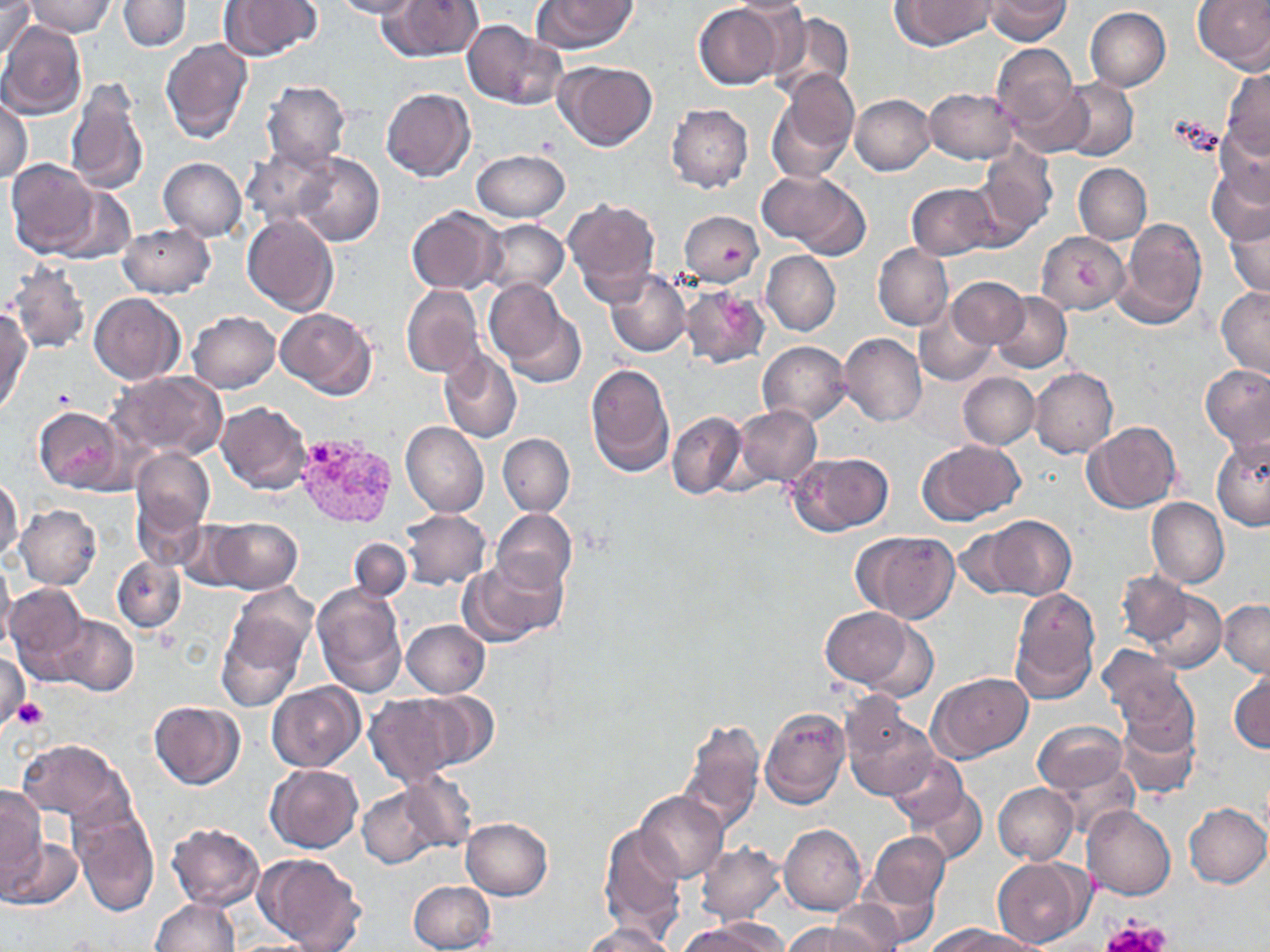 Approximate bounding boxes as [x1, y1, x2, y2] in pixels. Plasmodium vivax-infected red blood cell locations: [291, 432, 399, 531]. Platelet locations: [1173, 114, 1224, 156], [721, 242, 747, 271], [720, 299, 752, 331], [10, 697, 48, 728], [1103, 913, 1174, 952]. Uninfected red blood cell locations: [1, 0, 37, 64], [23, 0, 116, 37], [331, 0, 421, 19], [381, 0, 484, 62], [531, 0, 638, 54], [725, 0, 814, 18], [890, 0, 995, 50], [984, 0, 1070, 45], [1193, 0, 1270, 72], [118, 1, 190, 52], [219, 1, 321, 62], [694, 3, 785, 90], [1085, 6, 1171, 91], [767, 10, 855, 101], [0, 21, 87, 119], [461, 21, 565, 109], [160, 38, 252, 144], [992, 44, 1079, 136], [553, 61, 659, 152], [1221, 67, 1270, 157], [773, 69, 858, 173], [1058, 78, 1138, 162], [66, 79, 149, 195], [260, 81, 351, 169], [924, 87, 1019, 163], [381, 88, 475, 181], [850, 94, 936, 175], [0, 97, 32, 183], [667, 103, 753, 193], [1212, 122, 1270, 208], [975, 145, 1057, 240], [243, 146, 338, 227], [470, 150, 569, 222], [289, 151, 385, 246], [158, 157, 247, 241], [5, 159, 98, 258], [1208, 162, 1270, 246], [1073, 163, 1151, 244], [759, 168, 872, 260], [51, 184, 135, 265], [907, 184, 996, 259], [562, 198, 660, 304], [405, 207, 504, 293], [1224, 210, 1270, 298], [679, 211, 764, 287], [242, 214, 338, 317], [480, 217, 569, 296], [1114, 218, 1207, 328], [118, 223, 214, 298], [1037, 232, 1128, 315], [873, 243, 953, 331], [761, 250, 840, 336], [5, 263, 91, 355], [605, 269, 690, 357], [948, 277, 1029, 349], [483, 279, 586, 387], [1216, 284, 1270, 379], [401, 285, 483, 379], [679, 285, 771, 370], [991, 291, 1072, 373], [90, 293, 184, 384], [913, 305, 998, 388], [275, 307, 377, 399], [0, 310, 31, 414], [187, 311, 280, 392], [839, 333, 926, 426], [757, 341, 851, 424], [438, 348, 522, 443], [585, 363, 675, 475], [1201, 365, 1270, 454], [1029, 367, 1118, 458], [108, 371, 228, 460], [958, 372, 1039, 450], [214, 402, 312, 494], [34, 405, 125, 493], [732, 405, 821, 486], [667, 410, 747, 498], [1081, 421, 1182, 515], [401, 423, 489, 517], [497, 433, 574, 516], [1211, 437, 1270, 531], [918, 438, 1026, 524], [130, 447, 215, 538], [787, 451, 893, 536], [0, 476, 24, 564], [133, 497, 205, 571], [1146, 497, 1228, 589], [15, 503, 102, 589], [401, 508, 490, 590], [492, 510, 577, 592], [979, 515, 1076, 600], [208, 517, 302, 594], [174, 519, 254, 590], [954, 528, 1026, 598], [854, 530, 959, 624], [349, 538, 412, 602], [461, 556, 568, 644], [113, 558, 186, 633], [0, 561, 15, 653], [1117, 571, 1191, 646], [226, 583, 318, 673], [311, 583, 406, 697], [5, 584, 93, 684], [1143, 588, 1227, 673], [1010, 589, 1099, 701], [1218, 599, 1269, 677], [820, 606, 920, 690], [52, 616, 138, 696], [402, 620, 490, 698], [216, 624, 302, 711], [1099, 645, 1189, 726], [0, 652, 29, 732], [1230, 669, 1270, 755], [928, 672, 1033, 761], [266, 681, 364, 772], [414, 692, 498, 769], [363, 694, 468, 787], [840, 699, 936, 802], [149, 701, 244, 789], [760, 707, 850, 808], [1114, 712, 1198, 799], [678, 718, 764, 833], [1033, 721, 1126, 792], [17, 738, 127, 823], [887, 754, 971, 829], [1053, 756, 1138, 841], [265, 763, 363, 852], [397, 772, 478, 851], [993, 783, 1077, 864], [357, 786, 440, 867], [910, 786, 987, 867], [1, 787, 45, 885], [636, 790, 728, 883], [1184, 803, 1269, 887], [70, 804, 159, 916], [1083, 806, 1176, 900], [460, 818, 552, 900], [167, 823, 265, 911], [780, 823, 866, 914], [599, 824, 687, 940], [866, 832, 949, 912], [1, 835, 84, 910], [695, 843, 785, 924], [256, 853, 365, 951], [991, 856, 1092, 947], [858, 875, 939, 947], [408, 880, 495, 952], [151, 898, 238, 951], [827, 902, 907, 952], [683, 918, 786, 952], [787, 921, 875, 952], [584, 922, 676, 952], [930, 922, 1022, 952]. Slide-level diagnosis: Plasmodium vivax. Light microscopy. May-Grünwald-Giemsa-stained preparation. One field of a larger specimen. Image is 1270×952 pixels. 1000x magnification. Thin blood film.